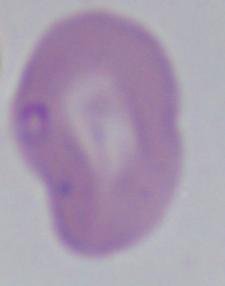
Summary:
  - Identification: Babesia
  - Modality: micrograph
  - Magnification: 1000x